Report the malaria status of this cell.
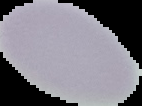
It is uninfected.

Summary:
  - Image type: segmented cell region on a black background
  - Preparation: thin blood film
  - Image size: 142×106 pixels